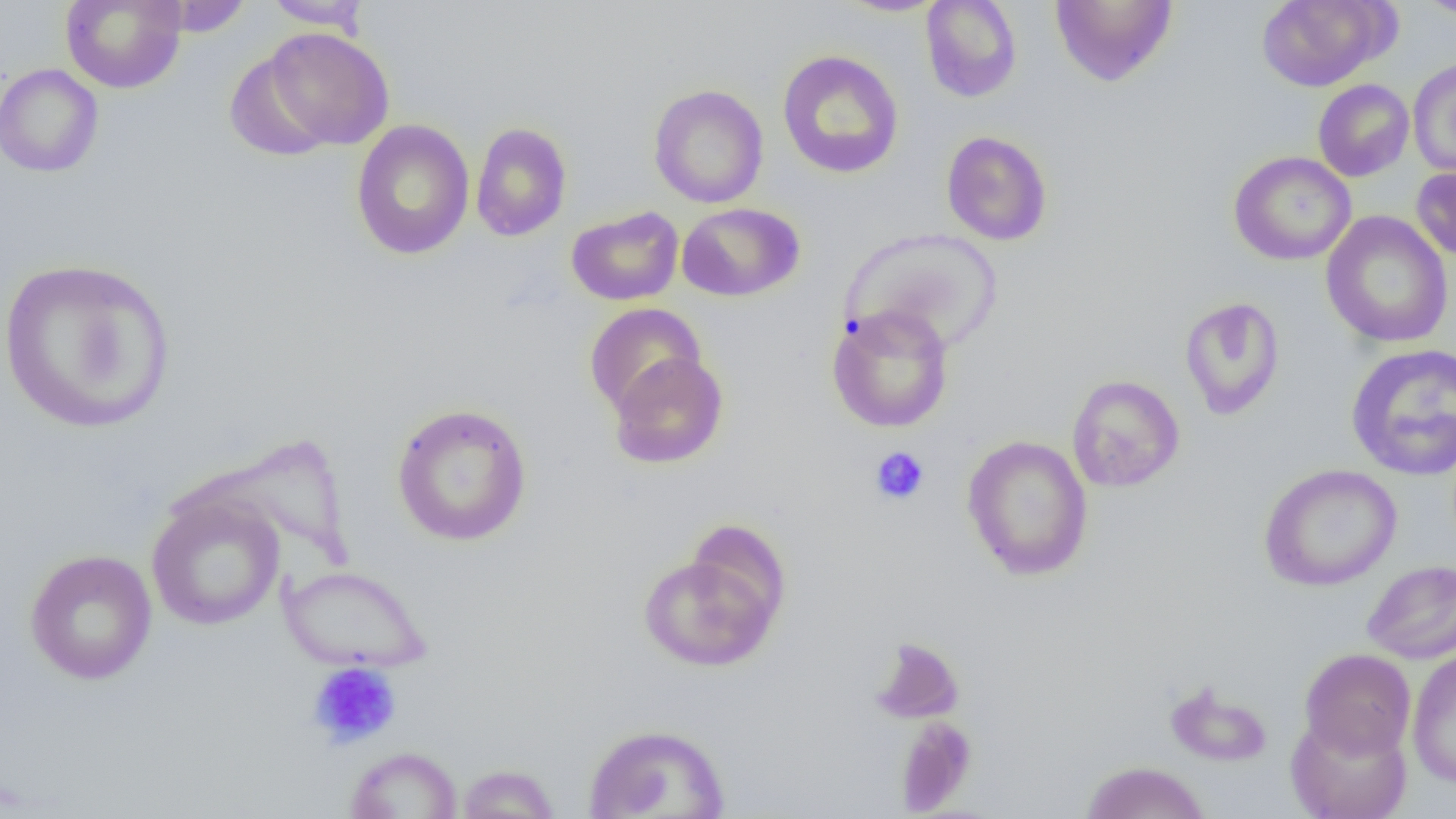
slide-level diagnosis = no evidence of blood parasites
uninfected red blood cell locations = approximate bounding boxes as [x1, y1, x2, y2] in pixels: [60, 0, 187, 93], [149, 0, 253, 36], [835, 0, 950, 17], [920, 0, 1023, 103], [1049, 0, 1178, 87], [1256, 0, 1393, 91], [1415, 0, 1455, 20], [263, 1, 372, 32], [260, 26, 396, 152], [776, 50, 904, 179], [1407, 57, 1456, 180], [0, 63, 104, 178], [1313, 78, 1414, 182], [648, 84, 769, 209], [350, 119, 475, 260], [470, 122, 572, 242], [940, 130, 1053, 246], [1228, 151, 1356, 266], [1411, 165, 1456, 263], [677, 202, 805, 302], [566, 206, 684, 306], [1320, 211, 1453, 348], [841, 227, 1002, 354], [0, 257, 177, 435], [1178, 296, 1285, 420], [585, 302, 707, 417], [827, 304, 955, 433], [1345, 343, 1456, 481], [606, 350, 729, 470], [1067, 374, 1184, 492], [390, 402, 533, 547], [961, 434, 1094, 581], [1259, 464, 1402, 591], [145, 493, 285, 632], [637, 545, 785, 673], [23, 548, 158, 685], [1361, 559, 1456, 664], [278, 564, 433, 673], [870, 636, 966, 725], [1299, 648, 1416, 760], [1406, 650, 1456, 789], [1164, 680, 1274, 767], [1286, 712, 1412, 819], [895, 717, 976, 815], [582, 723, 731, 818], [344, 746, 463, 818], [1079, 761, 1212, 819], [455, 763, 561, 818]
platelet locations = approximate bounding boxes as [x1, y1, x2, y2] in pixels: [868, 446, 931, 506], [306, 660, 402, 749]
magnification = 1000x
image size = 1456×819 pixels
field of view = single
preparation = thin blood film
modality = light microscopy